Which red blood cells are P. falciparum-infected, and which are of indeterminate infection status?
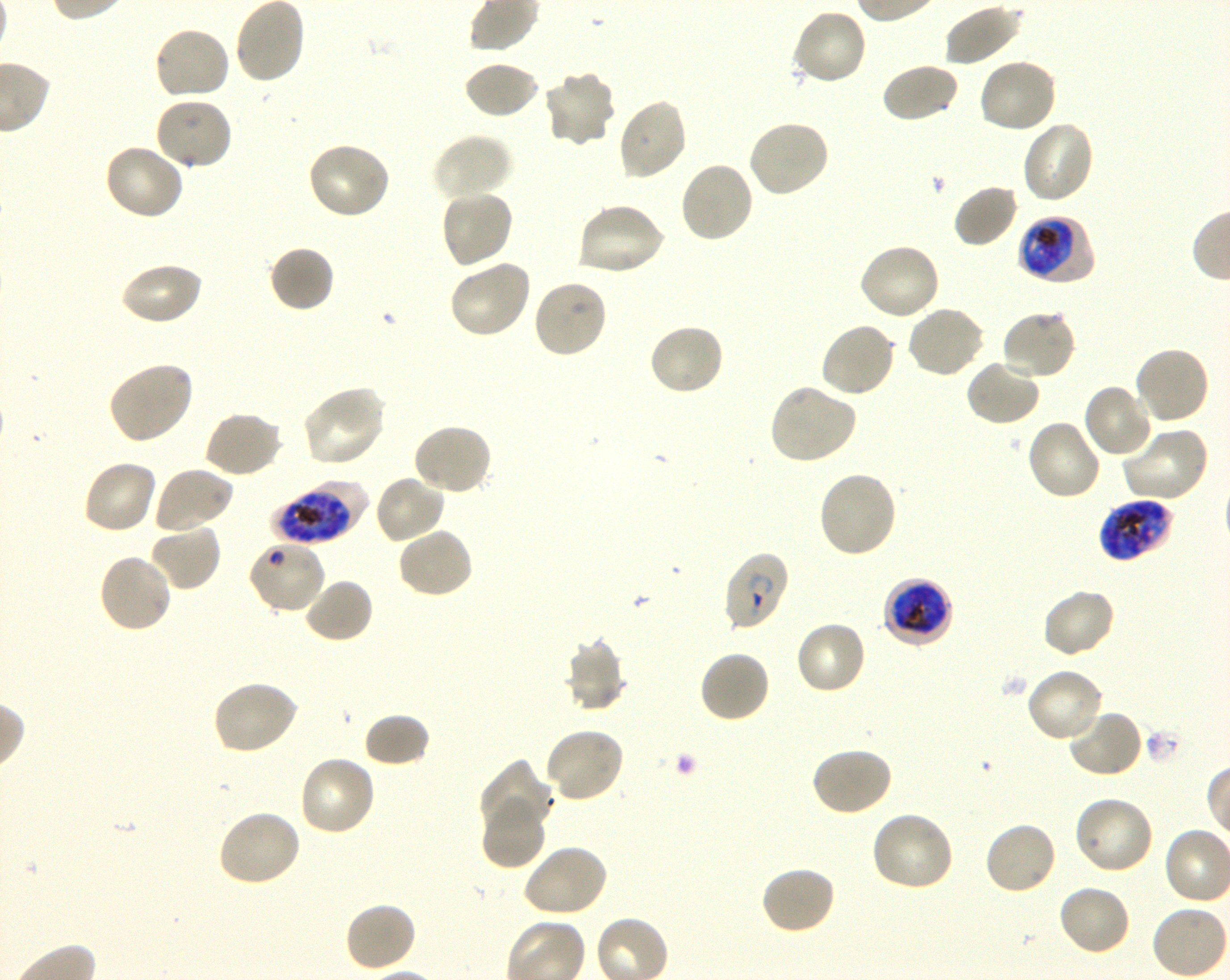
Approximate bounding boxes as (x1, y1, x2, y2) in pixels. Not every red blood cell is marked. A life-cycle stage — or a range of stages, where the recorded stages span more than one — follows each staged infected red blood cell.
Infected red blood cells: (1018, 214, 1097, 287) trophozoite; (273, 478, 366, 545) late trophozoite to late schizont; (1098, 498, 1175, 562) late trophozoite to late schizont; (722, 551, 790, 634) ring; (882, 577, 954, 648) late trophozoite to late schizont.
Red blood cells of indeterminate infection status: (247, 539, 327, 615).

Locations of uninfected red blood cells: (233, 0, 307, 85), (943, 4, 1023, 68), (790, 7, 868, 86), (152, 25, 232, 102), (977, 56, 1057, 135), (463, 59, 540, 119), (880, 62, 960, 124), (541, 71, 616, 148), (153, 95, 234, 172), (616, 97, 689, 182), (745, 119, 830, 199), (1020, 119, 1095, 204), (431, 133, 513, 202), (305, 141, 392, 221), (102, 142, 185, 221), (678, 161, 756, 244), (952, 183, 1019, 249), (439, 189, 514, 270), (576, 201, 667, 277), (857, 241, 941, 321), (268, 245, 335, 313), (447, 258, 532, 339), (119, 261, 203, 326), (532, 278, 609, 359), (905, 304, 986, 379), (1000, 309, 1077, 382), (647, 321, 726, 396), (819, 321, 898, 398), (1133, 345, 1210, 427), (965, 359, 1041, 427), (106, 361, 194, 445), (1081, 383, 1155, 460), (768, 384, 858, 466), (301, 385, 388, 468), (203, 410, 283, 479), (1024, 418, 1103, 502), (411, 422, 494, 496), (1120, 425, 1210, 504), (81, 458, 158, 535), (152, 466, 235, 535), (816, 469, 898, 559), (373, 473, 447, 544), (149, 523, 222, 592), (396, 526, 475, 599), (96, 552, 173, 634), (302, 578, 375, 645), (1040, 587, 1117, 658), (794, 621, 868, 697), (564, 636, 627, 713), (698, 650, 771, 725), (1024, 667, 1105, 744), (211, 680, 300, 756), (1066, 707, 1143, 779), (363, 713, 431, 768), (543, 727, 625, 805), (809, 746, 893, 817), (298, 755, 377, 838), (477, 757, 557, 838), (1071, 795, 1154, 876), (480, 800, 546, 870), (216, 807, 303, 887), (870, 810, 956, 893), (982, 820, 1058, 897), (521, 844, 609, 918), (760, 865, 837, 936), (1056, 883, 1132, 958), (344, 900, 417, 973). Life-cycle stages observed: ring, trophozoite. Blood group of the donor: O+. 100x objective under oil immersion, numerical aperture 1.30. Image is 1230×980 pixels. Thin blood film. Single field of view. Giemsa-stained preparation. P. falciparum strain 3D7 in shaking in-vitro culture.